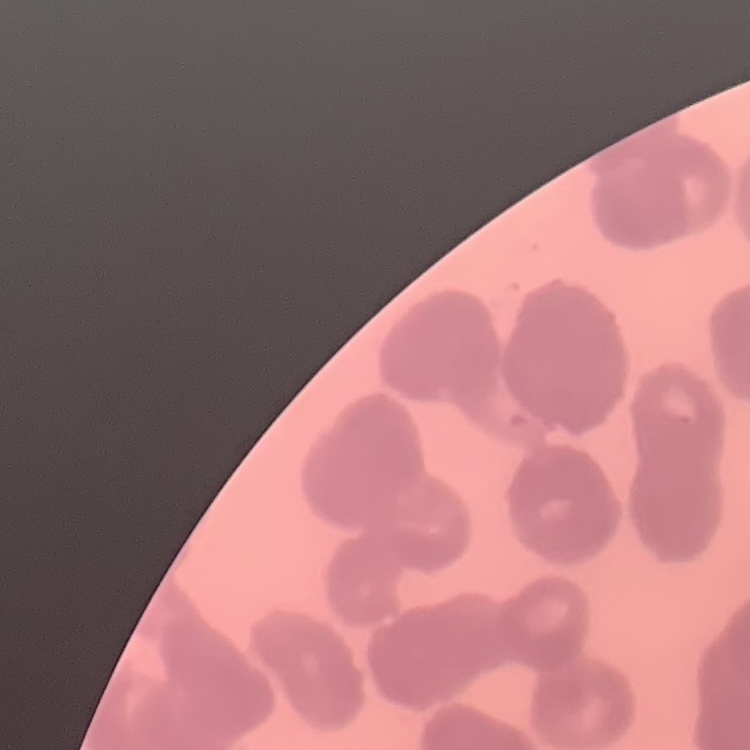
The red blood cells show rouleaux formation. One tile cut from a larger photomicrograph. Thin peripheral smear. Field's or Giemsa stain.